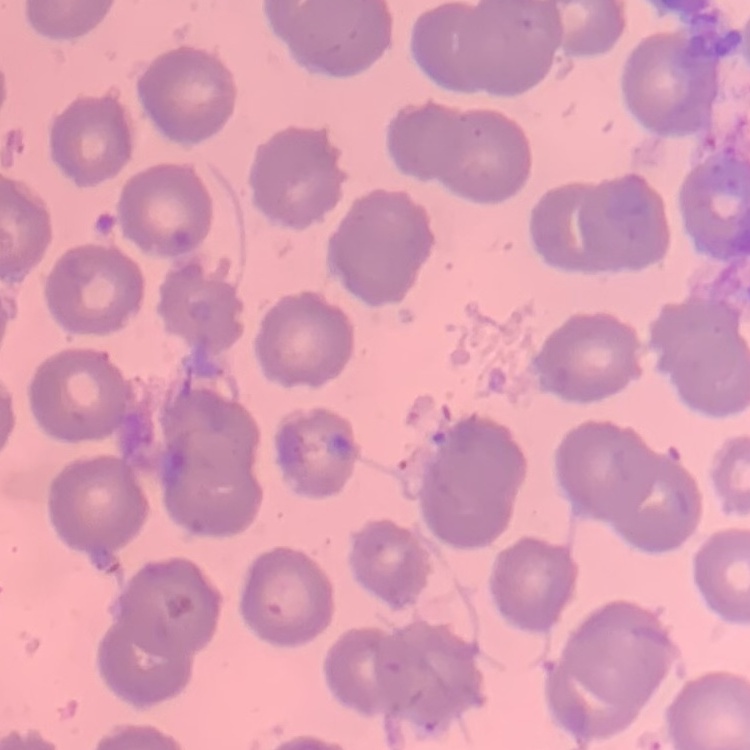

erythrocyte_morphology: no rouleaux formation
preparation: thin blood film
image_type: one tile cut from a larger photomicrograph
stain: Field's or Giemsa